Assess this cell for malaria.
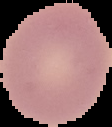

It is uninfected.

preparation = thin blood smear
image type = cell region segmented out of the field of view; surrounding area masked to black
image size = 112×127 pixels